State which parasite is depicted.
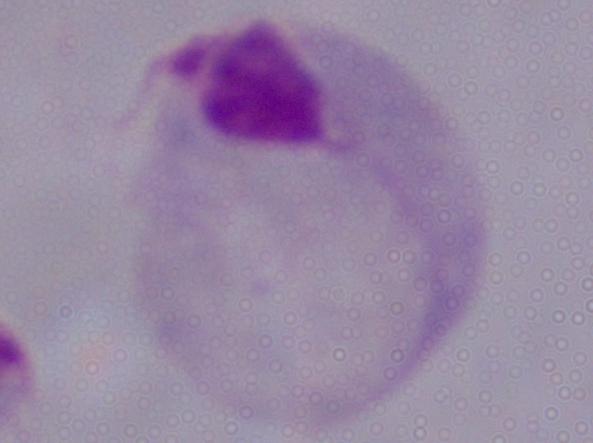

This is a trichomonad.

Micrograph. 1000x magnification.